Assess this cell for malaria.
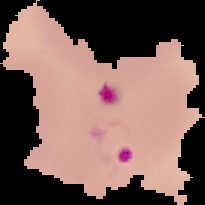

Parasitized.

From a thin blood film. Image is 205×205 pixels. Cell region segmented out of the field of view; the surrounding area is masked to black.